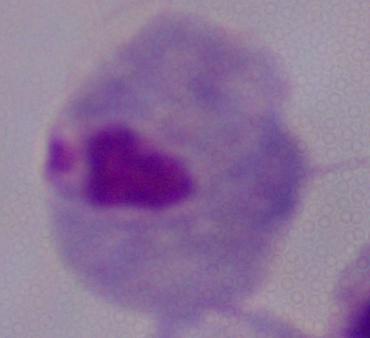

Summary:
  - Modality: photomicrograph
  - Identification: trichomonad
  - Magnification: 1000x